Name the parasite shown.
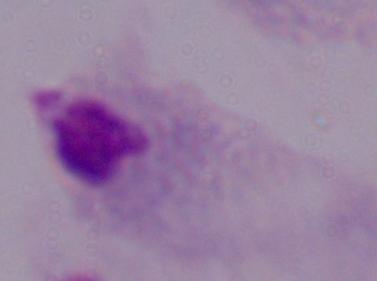
This is a trichomonad.

modality = micrograph
magnification = 1000x